Assess this cell for malaria.
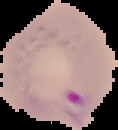
It is parasitized.

image size = 118×130 pixels
image type = segmented cell region on a black background
preparation = thin blood smear